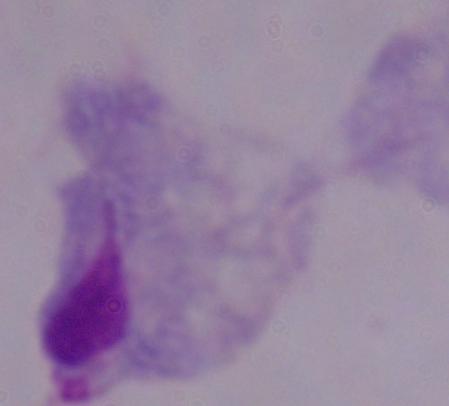

modality = micrograph
identification = trichomonad
magnification = 1000x